Assess this cell for malaria.
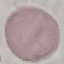
It is uninfected.

Photographed with a smartphone camera at the microscope eyepiece. Automatically extracted cell patch, resized to 64 × 64 pixels. Giemsa-stained preparation. Thin blood smear.